Point out every malaria parasite and every leukocyte.
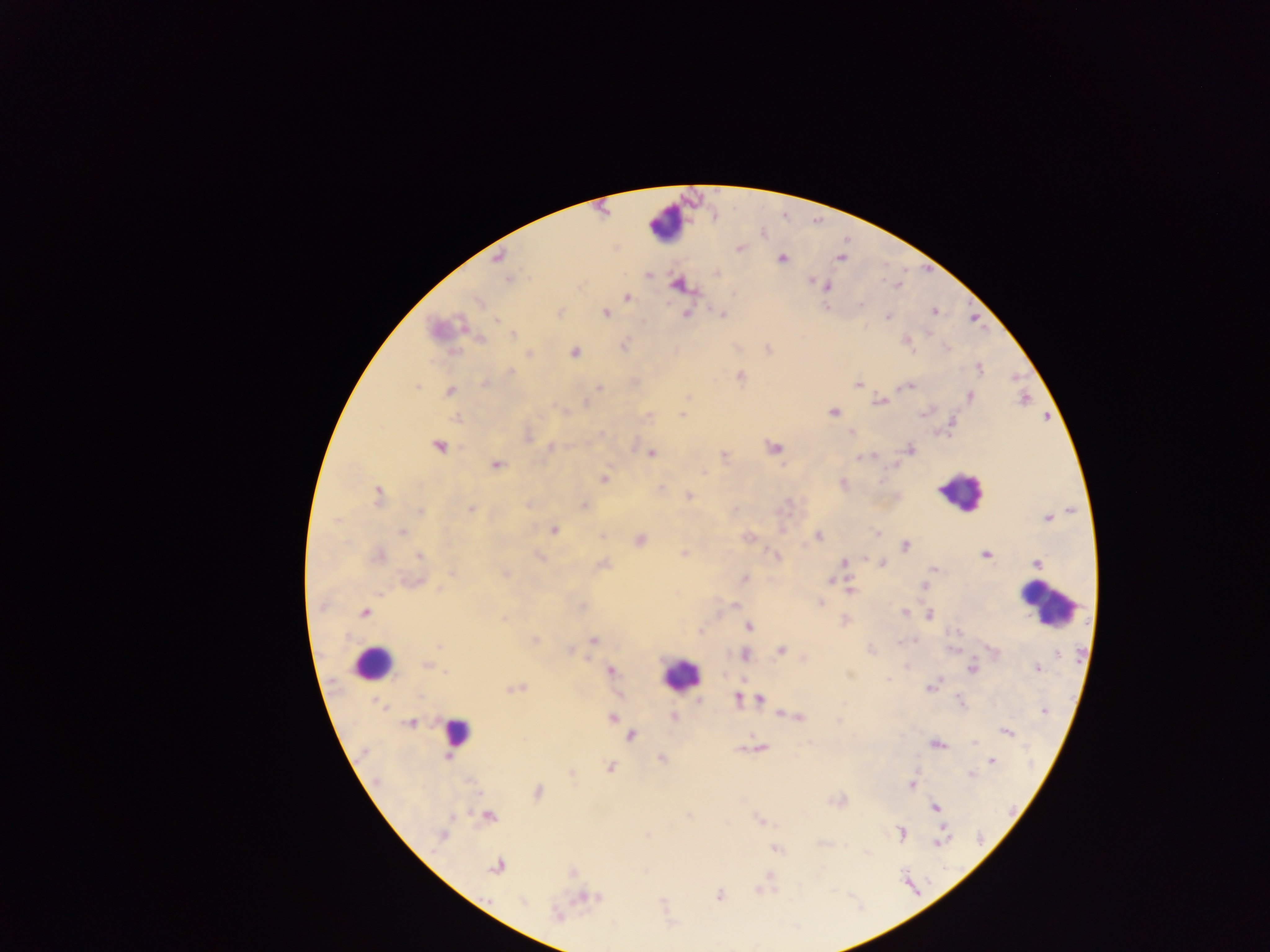
Approximate centers as [x, y] in pixels.
Malaria parasites: [739, 248], [499, 257], [781, 258], [839, 258], [647, 273], [717, 273], [508, 279], [813, 282], [677, 284], [827, 286], [626, 297], [478, 302], [861, 304], [559, 312], [933, 312], [605, 313], [686, 313], [722, 313], [887, 316], [496, 320], [442, 328], [512, 334], [480, 338], [905, 340], [624, 344], [768, 349], [453, 352], [574, 352], [528, 353], [979, 368], [511, 371], [739, 376], [485, 383], [858, 384], [416, 386], [906, 386], [599, 387], [450, 391], [969, 396], [687, 397], [880, 401], [584, 403], [563, 411], [833, 412], [924, 412], [683, 415], [454, 417], [852, 432], [527, 435], [439, 446], [551, 447], [773, 448], [909, 449], [651, 452], [870, 455], [864, 456], [724, 457], [495, 464], [605, 478], [842, 483], [660, 488], [377, 495], [688, 495], [528, 503], [582, 505], [471, 510], [420, 511], [1048, 518], [553, 529], [782, 529], [401, 532], [877, 534], [602, 535], [747, 536], [819, 536], [639, 540], [906, 546], [684, 553], [985, 554], [378, 555], [775, 555], [419, 556], [539, 556], [863, 559], [844, 561], [882, 562], [1037, 563], [602, 564], [933, 568], [451, 571], [504, 574], [744, 578], [830, 580], [412, 581], [924, 585], [441, 590], [850, 590], [820, 603], [734, 604], [582, 608], [365, 612], [905, 613], [929, 615], [504, 618], [844, 620], [748, 625], [700, 631], [956, 632], [534, 640], [593, 640], [439, 646], [569, 650], [780, 650], [993, 651], [1057, 653], [745, 654], [805, 658], [427, 665], [972, 668], [1037, 668], [610, 669], [445, 672], [933, 686], [515, 688], [619, 695], [737, 698], [699, 700], [759, 700], [381, 705], [1044, 711], [782, 712], [613, 717], [674, 717], [798, 717], [618, 721], [410, 723], [1007, 731], [631, 734], [935, 743], [759, 747], [741, 748], [447, 756], [661, 758], [991, 760], [610, 767], [571, 772], [971, 773], [912, 784], [537, 792], [935, 806], [488, 816], [760, 819], [900, 834], [441, 835], [647, 835], [939, 840], [775, 848], [496, 867], [572, 871], [759, 889], [718, 896], [590, 897], [523, 902], [557, 915].
Leukocytes: [666, 224], [960, 492], [1047, 605], [372, 663], [679, 674], [457, 732].

Thick blood film. One field of view. Image is 1270×952 pixels. Collected in Ghana. Photographed through a microscope with a mobile-phone camera.